State the blood parasite species.
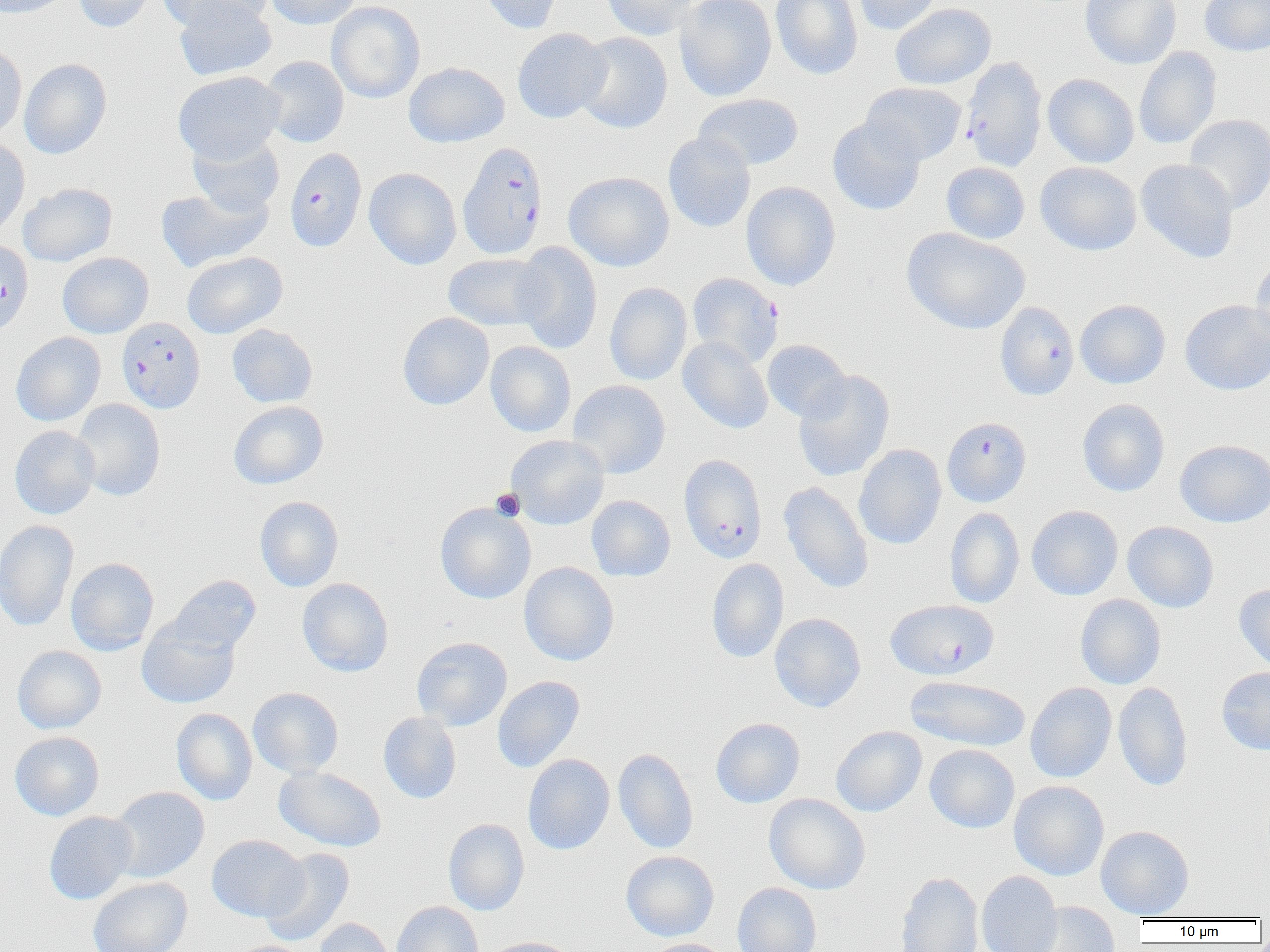

Plasmodium falciparum.

Approximate bounding boxes as (x1,y1)-(x2,y2) corner pairs in pixels. Platelet locations: (490,488)-(525,521). Uninfected red blood cell locations (subset): (0,0)-(72,18), (73,0)-(158,32), (160,0)-(272,31), (266,0)-(360,29), (478,0)-(564,35), (601,0)-(701,40), (674,0)-(777,101), (770,0)-(863,80), (852,0)-(943,35), (1081,0)-(1181,69), (1199,0)-(1270,56), (173,1)-(277,80), (327,1)-(425,103), (890,3)-(996,90), (513,28)-(611,123), (574,32)-(673,134), (0,40)-(27,142), (1133,46)-(1222,149), (260,56)-(349,148), (19,59)-(111,159), (173,71)-(285,163), (1043,74)-(1139,167), (861,82)-(967,164), (693,93)-(803,171), (1183,114)-(1270,214), (827,117)-(926,215), (663,132)-(755,232), (188,133)-(285,217), (0,136)-(30,239), (1135,159)-(1239,263), (1035,161)-(1142,256), (941,162)-(1030,244), (364,167)-(462,270), (563,172)-(674,271), (740,182)-(841,290), (18,183)-(117,266), (156,185)-(272,272), (902,227)-(1030,334), (512,242)-(603,354), (182,251)-(287,338), (1250,252)-(1270,352), (57,253)-(154,338), (443,253)-(551,330), (605,282)-(692,386), (1075,300)-(1171,388), (1180,300)-(1270,395), (397,312)-(494,410), (226,324)-(318,407), (11,332)-(106,426), (678,336)-(774,434), (762,339)-(851,422), (485,341)-(576,437), (793,370)-(895,482), (568,380)-(670,478), (71,398)-(166,501), (1077,398)-(1170,497), (228,400)-(328,489), (9,426)-(100,519), (505,435)-(609,530), (1174,439)-(1270,527), (854,444)-(946,550), (779,481)-(874,593), (586,495)-(675,581), (255,496)-(344,592), (435,502)-(536,604), (1026,505)-(1123,600), (944,507)-(1025,609), (0,519)-(79,632), (1122,521)-(1219,612), (65,557)-(159,655), (707,558)-(789,663), (519,562)-(619,666), (166,575)-(261,655), (296,577)-(394,677), (1234,582)-(1270,675), (1075,594)-(1166,689), (769,612)-(866,712), (137,618)-(240,709), (411,636)-(512,731), (12,645)-(106,734), (1216,667)-(1270,754), (905,675)-(1031,752), (492,676)-(585,772), (1025,682)-(1117,783), (1113,682)-(1193,792), (247,687)-(344,778), (171,708)-(257,805), (378,712)-(462,804), (711,717)-(805,808), (831,726)-(927,817), (9,731)-(104,821), (830,738)-(1019,821), (924,744)-(1019,833), (613,748)-(698,854), (523,754)-(614,855), (274,765)-(387,852), (1008,780)-(1109,880), (109,786)-(210,882), (764,794)-(870,894), (43,811)-(138,905), (443,818)-(529,915), (1096,825)-(1194,918), (206,835)-(308,922), (260,848)-(355,947), (621,850)-(720,941), (895,870)-(983,952), (976,871)-(1062,952), (88,876)-(192,952), (732,882)-(822,952), (392,901)-(484,952), (1027,902)-(1121,951), (314,918)-(396,952), (481,936)-(578,952), (640,938)-(734,952), (226,940)-(319,952). Plasmodium falciparum-infected red blood cell locations (subset): (960,56)-(1047,172), (402,62)-(508,149), (457,142)-(549,260), (284,148)-(367,252), (0,239)-(33,336), (686,273)-(782,368), (994,302)-(1079,401), (116,318)-(205,413), (942,416)-(1032,507), (678,454)-(767,562). Captured at 1000x magnification. Optical microscopy. One field of a larger specimen. Thin blood film. Image is 1270×952 pixels.